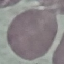
Summary:
  - Malaria status: uninfected
  - Stain: Giemsa
  - Preparation: thin blood smear
  - Capture: smartphone camera at the microscope eyepiece
  - Image type: automatically extracted cell patch, resized to 64 × 64 pixels